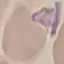

{
  "result": "no malaria parasites seen",
  "capture": "smartphone camera at the microscope eyepiece",
  "preparation": "thin blood film",
  "image_type": "cell patch, automatically extracted from a larger field of view and resized to 64 × 64 pixels",
  "stain": "Giemsa"
}